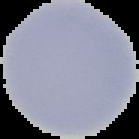

Malaria status: uninfected. Cell region segmented out of the field of view; the surrounding area is masked to black. Image is 139×139 pixels. From a thin blood smear.